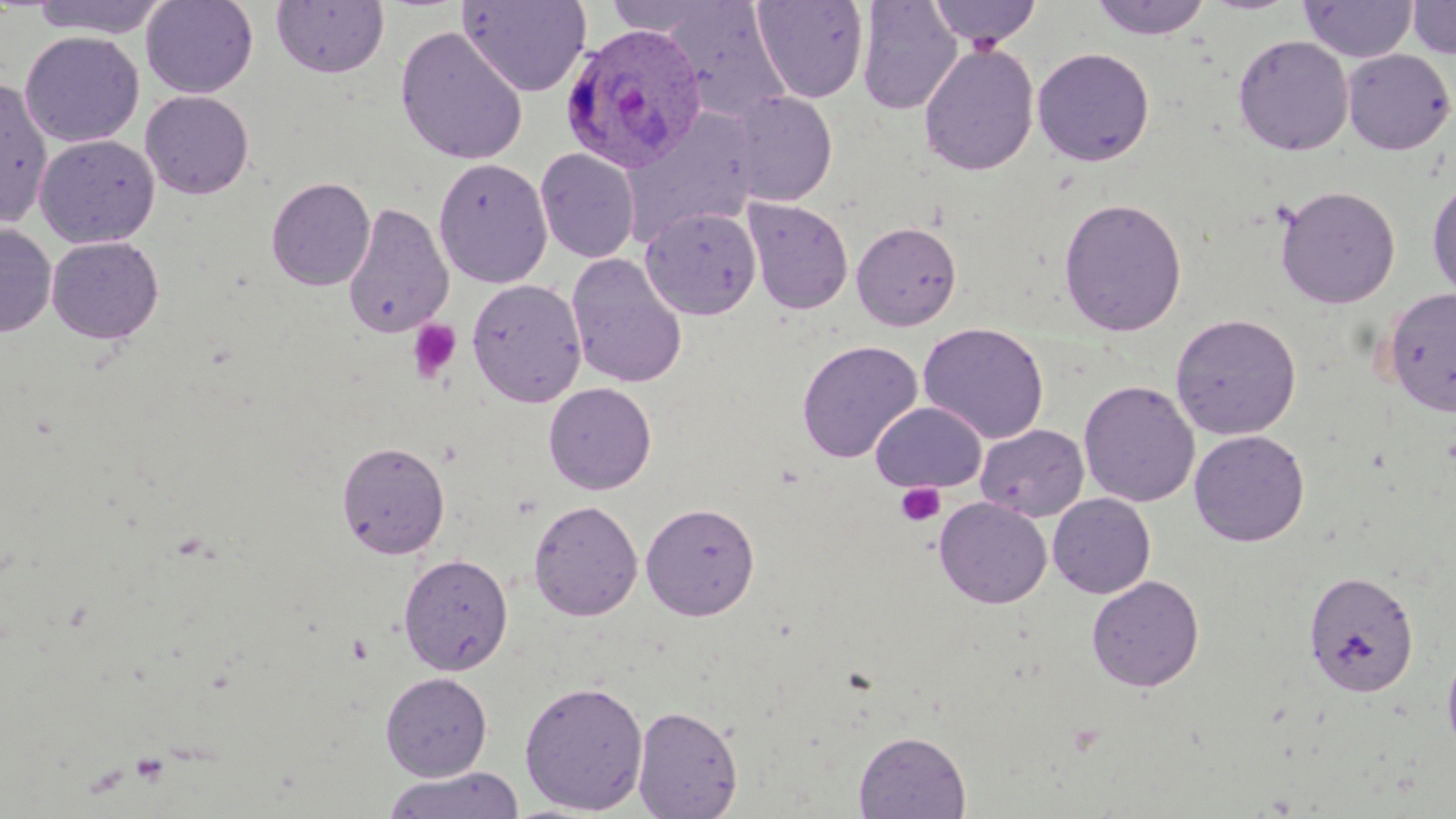
Summary:
  - Coordinate format: approximate bounding boxes as named x1/y1/x2/y2 corners in pixels
  - Uninfected red blood cell locations: (x1=29, y1=0, x2=172, y2=39), (x1=140, y1=0, x2=258, y2=99), (x1=271, y1=0, x2=389, y2=78), (x1=458, y1=0, x2=592, y2=97), (x1=604, y1=0, x2=727, y2=37), (x1=750, y1=0, x2=870, y2=104), (x1=856, y1=0, x2=963, y2=115), (x1=927, y1=0, x2=1043, y2=50), (x1=1089, y1=0, x2=1212, y2=41), (x1=1300, y1=0, x2=1417, y2=63), (x1=1407, y1=0, x2=1456, y2=60), (x1=662, y1=2, x2=792, y2=123), (x1=395, y1=26, x2=528, y2=166), (x1=19, y1=31, x2=144, y2=147), (x1=1232, y1=34, x2=1353, y2=155), (x1=918, y1=43, x2=1040, y2=177), (x1=1032, y1=47, x2=1155, y2=166), (x1=1341, y1=48, x2=1455, y2=155), (x1=0, y1=78, x2=53, y2=230), (x1=140, y1=91, x2=254, y2=199), (x1=726, y1=91, x2=838, y2=207), (x1=623, y1=111, x2=759, y2=242), (x1=35, y1=134, x2=159, y2=248), (x1=535, y1=148, x2=640, y2=263), (x1=433, y1=157, x2=552, y2=289), (x1=266, y1=175, x2=375, y2=291), (x1=1427, y1=178, x2=1456, y2=302), (x1=1275, y1=186, x2=1401, y2=309), (x1=1058, y1=196, x2=1188, y2=337), (x1=742, y1=197, x2=854, y2=315), (x1=342, y1=200, x2=454, y2=339), (x1=640, y1=206, x2=761, y2=320), (x1=851, y1=221, x2=962, y2=331), (x1=0, y1=224, x2=57, y2=337), (x1=46, y1=236, x2=164, y2=344), (x1=566, y1=253, x2=688, y2=389), (x1=467, y1=277, x2=587, y2=407), (x1=1381, y1=287, x2=1456, y2=416), (x1=1169, y1=312, x2=1302, y2=440), (x1=917, y1=322, x2=1050, y2=444), (x1=796, y1=339, x2=923, y2=463), (x1=1079, y1=380, x2=1200, y2=507), (x1=542, y1=382, x2=657, y2=495), (x1=871, y1=401, x2=988, y2=493), (x1=975, y1=423, x2=1090, y2=522), (x1=1189, y1=429, x2=1310, y2=546), (x1=336, y1=440, x2=450, y2=559), (x1=1048, y1=494, x2=1156, y2=599), (x1=934, y1=497, x2=1052, y2=609), (x1=528, y1=499, x2=643, y2=621), (x1=640, y1=501, x2=760, y2=620), (x1=398, y1=552, x2=514, y2=676), (x1=1303, y1=569, x2=1420, y2=697), (x1=1086, y1=575, x2=1205, y2=692), (x1=1441, y1=641, x2=1456, y2=757), (x1=380, y1=672, x2=492, y2=780), (x1=519, y1=680, x2=649, y2=814), (x1=633, y1=705, x2=742, y2=818), (x1=854, y1=730, x2=971, y2=818), (x1=380, y1=765, x2=526, y2=819)
  - Plasmodium ovale-infected red blood cell locations: (x1=560, y1=23, x2=708, y2=173)
  - Platelet locations: (x1=407, y1=319, x2=463, y2=384), (x1=895, y1=482, x2=946, y2=527)
  - Slide-level diagnosis: Plasmodium ovale
  - Field of view: single
  - Stain: May-Grünwald-Giemsa
  - Modality: optical microscopy
  - Preparation: thin blood smear
  - Image size: 1456×819 pixels
  - Magnification: 1000x